Locate every blood parasite and identify its species.
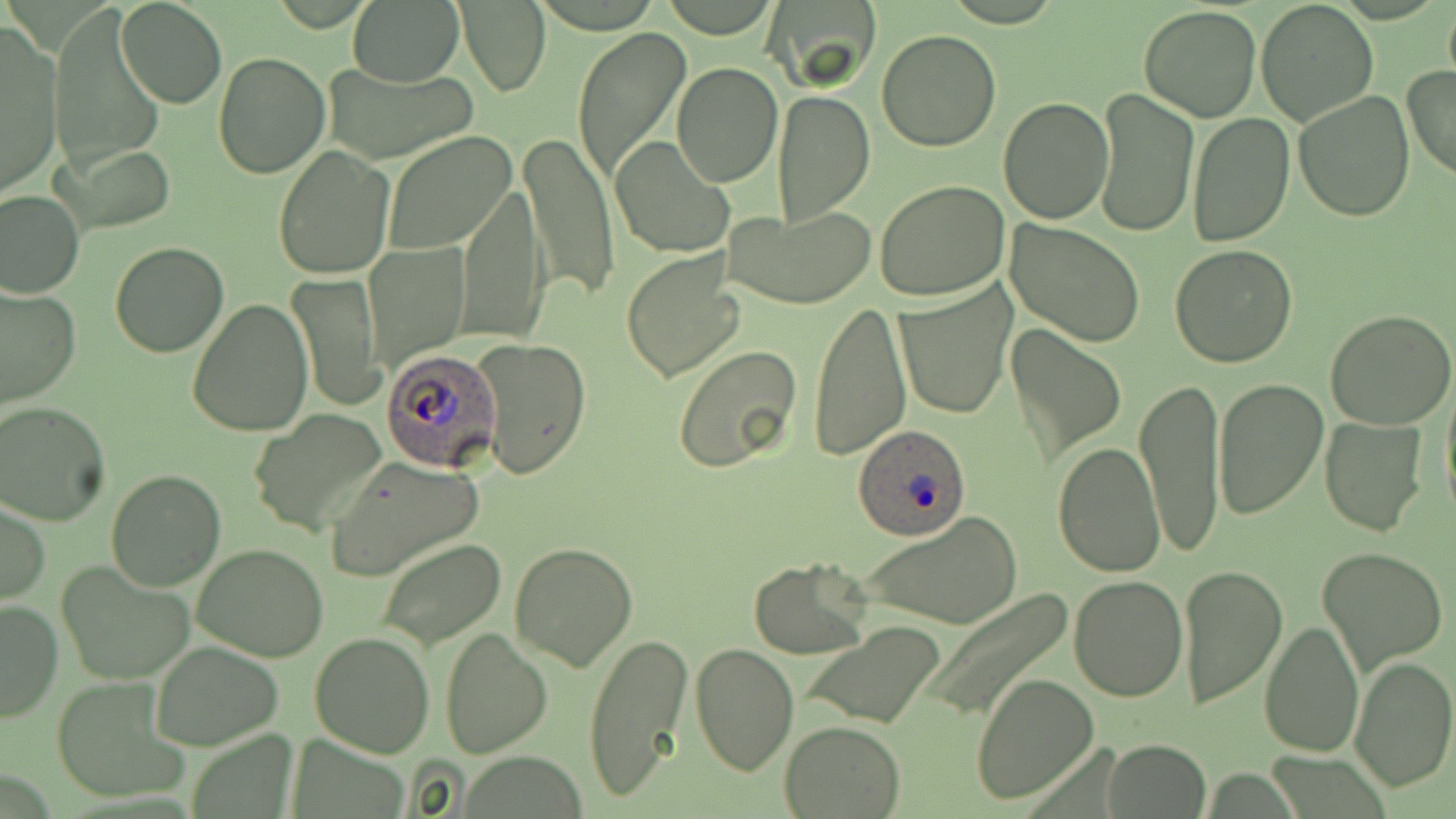

Approximate bounding boxes as (x1, y1, x2, y2) in pixels.
Plasmodium ovale-infected red blood cells: (378, 348, 498, 472), (850, 425, 972, 541).
No Plasmodium falciparum, Plasmodium malariae, Plasmodium vivax, Babesia divergens, or Trypanosoma brucei observed.

Uninfected red blood cell locations: (348, 0, 465, 88), (765, 0, 879, 89), (1256, 0, 1379, 126), (115, 1, 226, 109), (1442, 2, 1456, 91), (458, 3, 550, 96), (1138, 5, 1262, 123), (50, 7, 165, 177), (1, 26, 62, 197), (573, 26, 691, 184), (876, 29, 1003, 151), (213, 54, 330, 178), (324, 62, 478, 162), (670, 62, 782, 187), (1403, 66, 1456, 183), (1093, 86, 1198, 237), (772, 90, 875, 224), (1294, 90, 1415, 223), (998, 96, 1114, 225), (1187, 110, 1295, 247), (382, 130, 519, 255), (520, 132, 619, 303), (609, 137, 735, 260), (62, 144, 177, 234), (273, 145, 395, 281), (875, 180, 1011, 302), (458, 182, 546, 347), (0, 187, 84, 298), (723, 203, 876, 309), (1005, 221, 1144, 346), (365, 240, 469, 369), (109, 242, 229, 358), (1168, 245, 1298, 368), (620, 249, 746, 382), (289, 273, 382, 411), (893, 283, 1015, 419), (1, 285, 79, 410), (186, 298, 311, 437), (809, 300, 910, 463), (1326, 307, 1456, 429), (1006, 323, 1126, 463), (474, 337, 591, 481), (673, 346, 804, 474), (1440, 373, 1456, 522), (1135, 377, 1227, 556), (1210, 377, 1327, 521), (0, 401, 109, 525), (248, 409, 387, 538), (1320, 416, 1427, 536), (1052, 441, 1165, 578), (326, 458, 482, 580), (106, 469, 228, 591), (0, 500, 49, 606), (859, 509, 1024, 630), (375, 538, 507, 648), (508, 539, 638, 671), (193, 544, 331, 662), (1316, 546, 1448, 675), (748, 557, 874, 657), (55, 562, 195, 686), (1177, 564, 1288, 710), (1067, 574, 1187, 702), (924, 590, 1075, 720), (0, 597, 62, 722), (1259, 619, 1365, 757), (799, 622, 947, 729), (440, 625, 553, 758), (583, 630, 693, 803), (310, 632, 435, 756), (148, 640, 284, 750), (690, 642, 798, 777), (1349, 655, 1456, 793), (971, 673, 1099, 806), (50, 678, 189, 805), (779, 720, 905, 817), (1102, 740, 1210, 818). Slide-level diagnosis: Plasmodium ovale. 1000x magnification. Single field of view. Image is 1456×819 pixels. May-Grünwald-Giemsa stain. Thin blood smear. Optical microscopy.